Identify the blood parasite species.
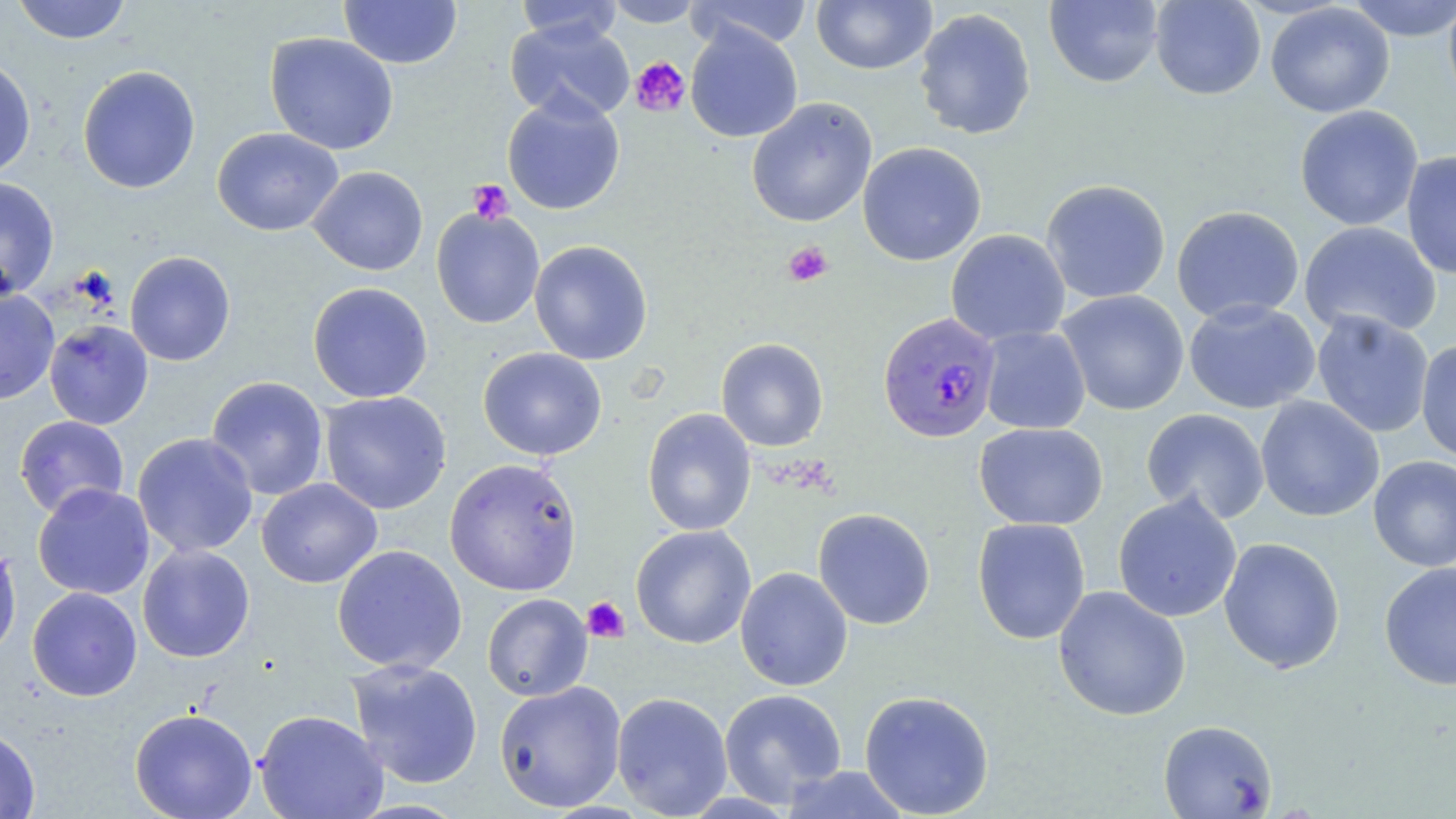

Plasmodium falciparum.

Summary:
  - Coordinate format: approximate bounding boxes as [x1, y1, x2, y2] in pixels
  - Platelet locations: [629, 56, 692, 117], [468, 179, 514, 224], [783, 241, 834, 287], [582, 596, 629, 643]
  - Plasmodium falciparum-infected red blood cell locations: [877, 311, 1001, 443]
  - Uninfected red blood cell locations: [12, 0, 131, 44], [339, 0, 462, 69], [602, 0, 705, 27], [811, 0, 936, 74], [1045, 0, 1164, 88], [1150, 0, 1266, 100], [1343, 0, 1456, 41], [1443, 0, 1456, 114], [515, 1, 623, 47], [688, 1, 814, 51], [1265, 3, 1395, 118], [914, 7, 1037, 140], [505, 19, 635, 123], [685, 23, 803, 142], [264, 32, 399, 155], [0, 56, 36, 181], [77, 65, 200, 194], [502, 94, 625, 215], [746, 98, 878, 227], [1295, 105, 1423, 231], [211, 127, 343, 236], [857, 142, 987, 266], [1402, 151, 1456, 280], [308, 166, 428, 276], [0, 177, 60, 299], [1041, 179, 1171, 304], [1171, 205, 1304, 325], [430, 207, 545, 329], [1299, 221, 1442, 339], [945, 229, 1070, 346], [529, 240, 653, 364], [125, 250, 236, 366], [307, 282, 433, 403], [0, 288, 60, 405], [1056, 290, 1189, 416], [1184, 300, 1321, 414], [1312, 310, 1434, 438], [44, 319, 154, 430], [978, 325, 1091, 434], [716, 338, 828, 451], [1416, 340, 1456, 464], [478, 347, 607, 461], [206, 376, 329, 501], [320, 391, 452, 515], [1255, 396, 1384, 522], [642, 408, 756, 536], [1141, 408, 1270, 524], [14, 415, 129, 518], [974, 422, 1108, 530], [132, 432, 258, 558], [1368, 455, 1456, 572], [444, 457, 582, 596], [257, 478, 382, 588], [32, 482, 155, 600], [1113, 492, 1242, 622], [813, 508, 936, 630], [972, 517, 1091, 645], [630, 524, 756, 649], [1218, 537, 1345, 674], [0, 540, 21, 661], [137, 544, 255, 662], [332, 544, 467, 674], [1379, 562, 1456, 690], [735, 567, 852, 691], [1052, 585, 1191, 721], [27, 587, 142, 701], [482, 593, 592, 701], [346, 658, 484, 790], [494, 680, 626, 813], [719, 688, 847, 807], [859, 690, 995, 818], [612, 692, 732, 817], [129, 707, 258, 819], [254, 709, 388, 819], [1158, 719, 1277, 818], [0, 726, 40, 818], [779, 765, 912, 818]
  - Field of view: single
  - Modality: optical microscopy
  - Preparation: thin blood smear
  - Stain: May-Grünwald-Giemsa
  - Magnification: 1000x
  - Image size: 1456×819 pixels